Identify the parasite.
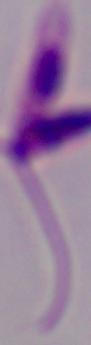
This is Leishmania.

Summary:
  - Magnification: 1000x
  - Modality: micrograph